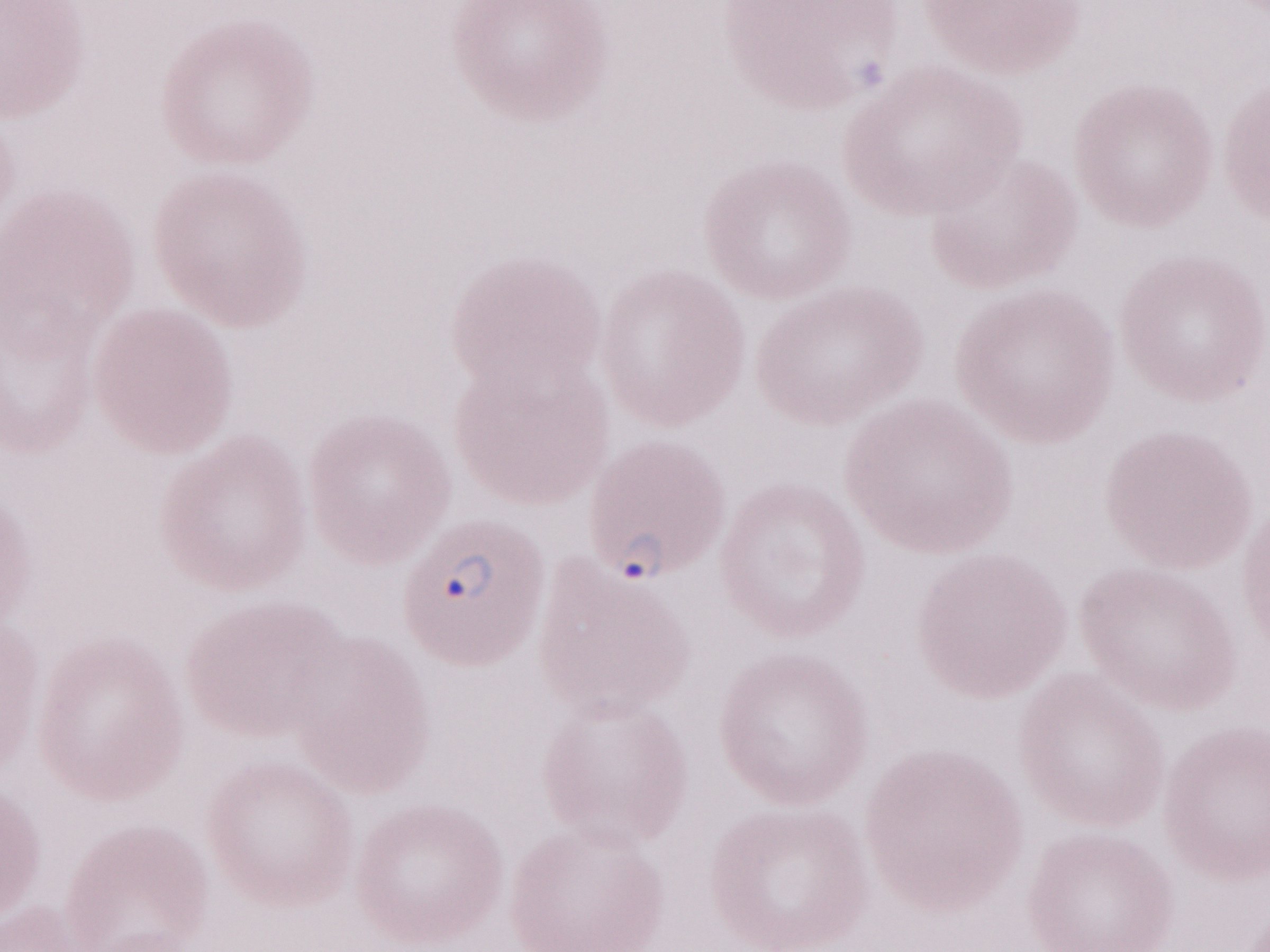
May-Grünwald-Giemsa (MGG) stain. Image is 1270×952 pixels. Patient diagnosis: malaria infection. One field of this slide. Olympus BX43 microscope and DP73 digital camera. Magnification: 1,000x. Thin peripheral-blood smear.